Locate every Plasmodium falciparum-infected red blood cell.
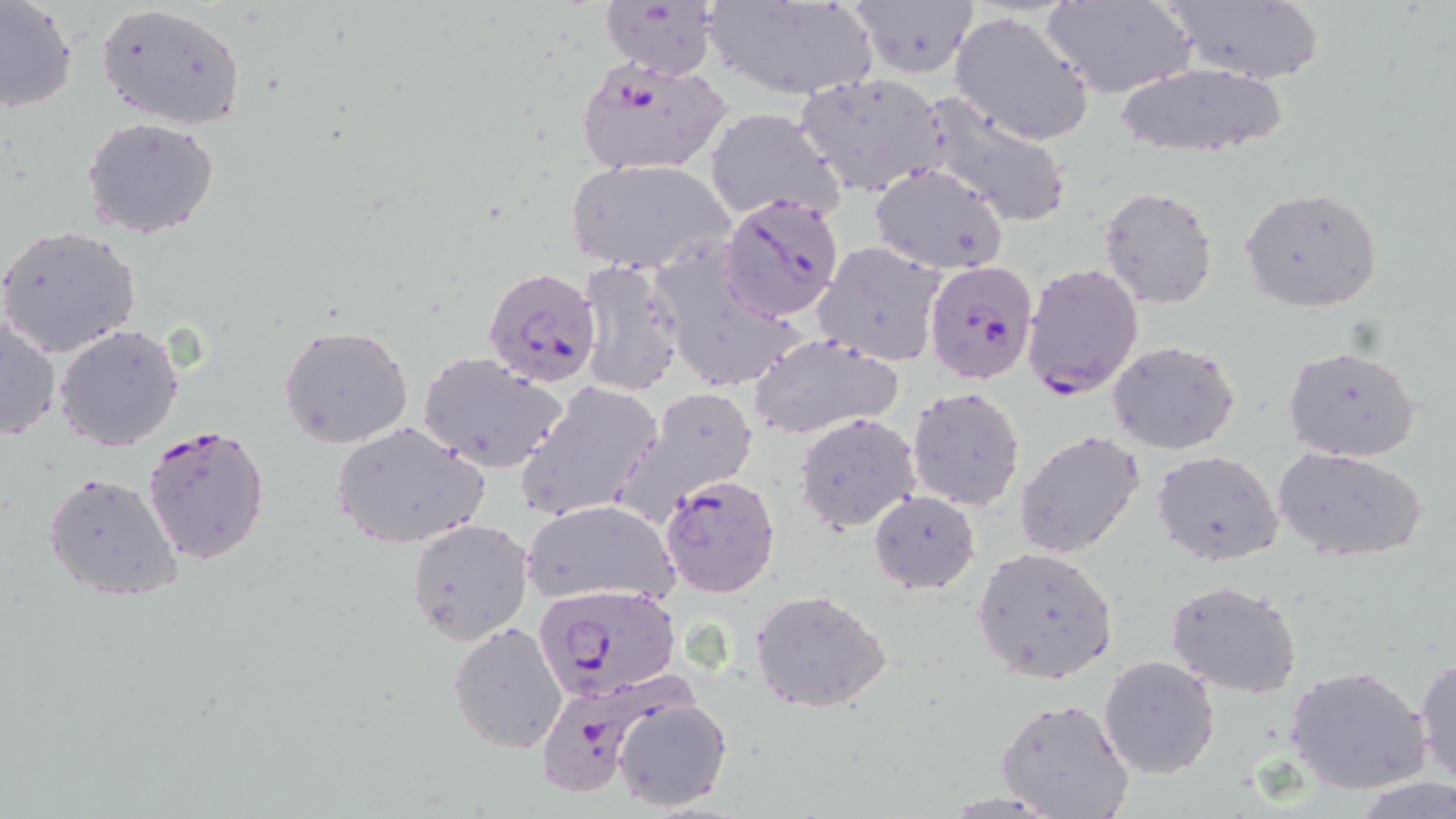

Approximate bounding boxes as [x1, y1, x2, y2] in pixels.
Plasmodium falciparum-infected red blood cells: [574, 54, 731, 177], [718, 194, 843, 321], [924, 260, 1038, 387], [1022, 262, 1145, 401], [482, 267, 602, 388], [141, 423, 270, 565], [660, 472, 781, 598], [534, 582, 681, 702], [530, 678, 670, 803].

slide-level diagnosis = Plasmodium falciparum
stain = May-Grünwald-Giemsa
uninfected red blood cell locations = approximate bounding boxes as [x1, y1, x2, y2] in pixels: [1, 0, 77, 114], [703, 0, 877, 101], [847, 0, 980, 80], [1042, 0, 1196, 100], [1162, 0, 1325, 86], [597, 2, 723, 81], [95, 3, 245, 131], [948, 11, 1096, 147], [1108, 60, 1291, 162], [793, 70, 950, 197], [917, 92, 1074, 228], [703, 108, 846, 224], [81, 118, 221, 240], [566, 158, 733, 276], [868, 162, 1008, 273], [1097, 185, 1220, 310], [1240, 186, 1384, 312], [0, 225, 142, 360], [814, 241, 947, 366], [649, 247, 806, 393], [576, 258, 686, 397], [0, 315, 61, 443], [279, 322, 413, 450], [54, 323, 185, 450], [748, 332, 904, 440], [1106, 339, 1242, 456], [1283, 342, 1422, 462], [417, 351, 569, 471], [516, 380, 664, 524], [620, 385, 759, 514], [907, 386, 1025, 511], [795, 413, 922, 535], [331, 419, 487, 552], [1014, 430, 1145, 558], [1273, 447, 1430, 562], [1154, 451, 1284, 567], [43, 470, 184, 602], [869, 490, 981, 593], [521, 499, 677, 607], [405, 518, 534, 647], [972, 546, 1117, 683], [1165, 579, 1303, 698], [751, 590, 893, 714], [448, 619, 569, 755], [1098, 654, 1220, 777], [1413, 654, 1456, 788], [1286, 665, 1431, 796], [993, 697, 1132, 819], [613, 698, 733, 813], [1355, 778, 1456, 818]
modality = light microscopy
preparation = thin blood smear
magnification = 1000x
image size = 1456×819 pixels
field of view = single